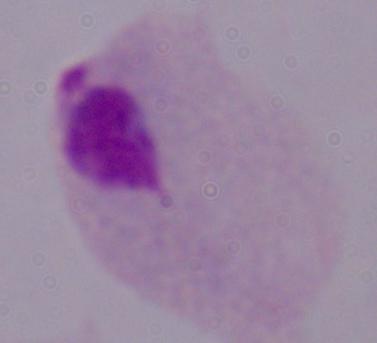

A trichomonad is shown. Captured at 1000x magnification. Micrograph.